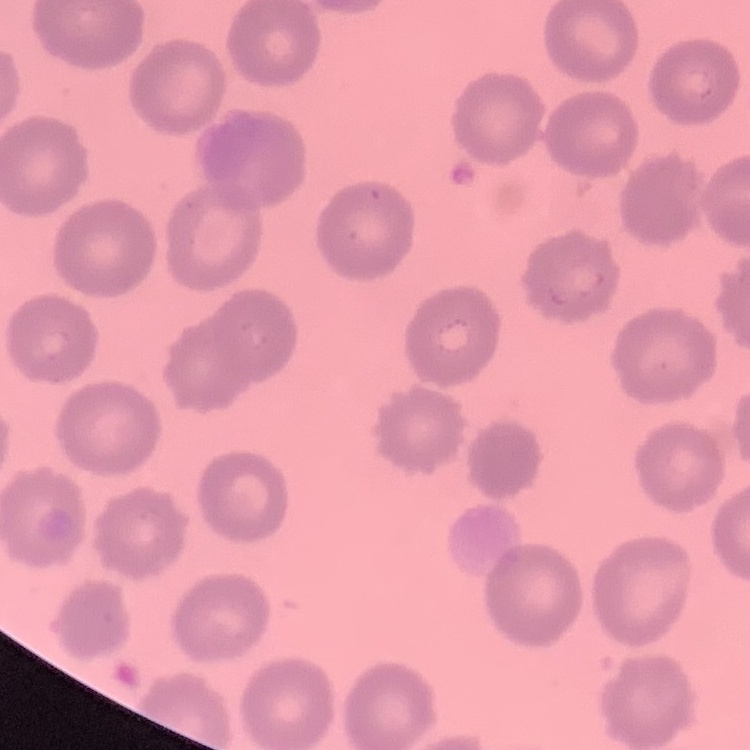

red_blood_cell_morphology: no rouleaux formation
image_type: square crop of a larger photomicrograph
stain: Field's or Giemsa
preparation: thin peripheral smear